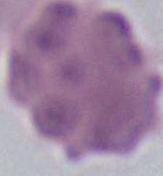
Summary:
  - Identification: erythrocyte
  - Magnification: 1000x
  - Modality: micrograph